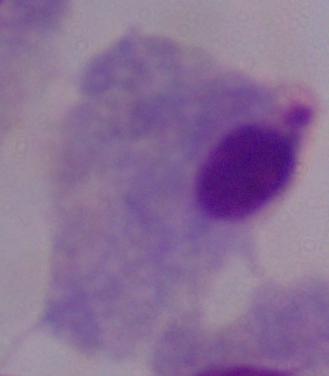

Summary:
  - Magnification: 1000x
  - Identification: trichomonad
  - Modality: micrograph